Report the malaria status of this cell.
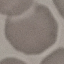
Uninfected.

capture = smartphone camera at the microscope eyepiece
image type = cell patch, automatically extracted from a larger field of view and resized to 64 × 64 pixels
stain = Giemsa
preparation = thin blood smear